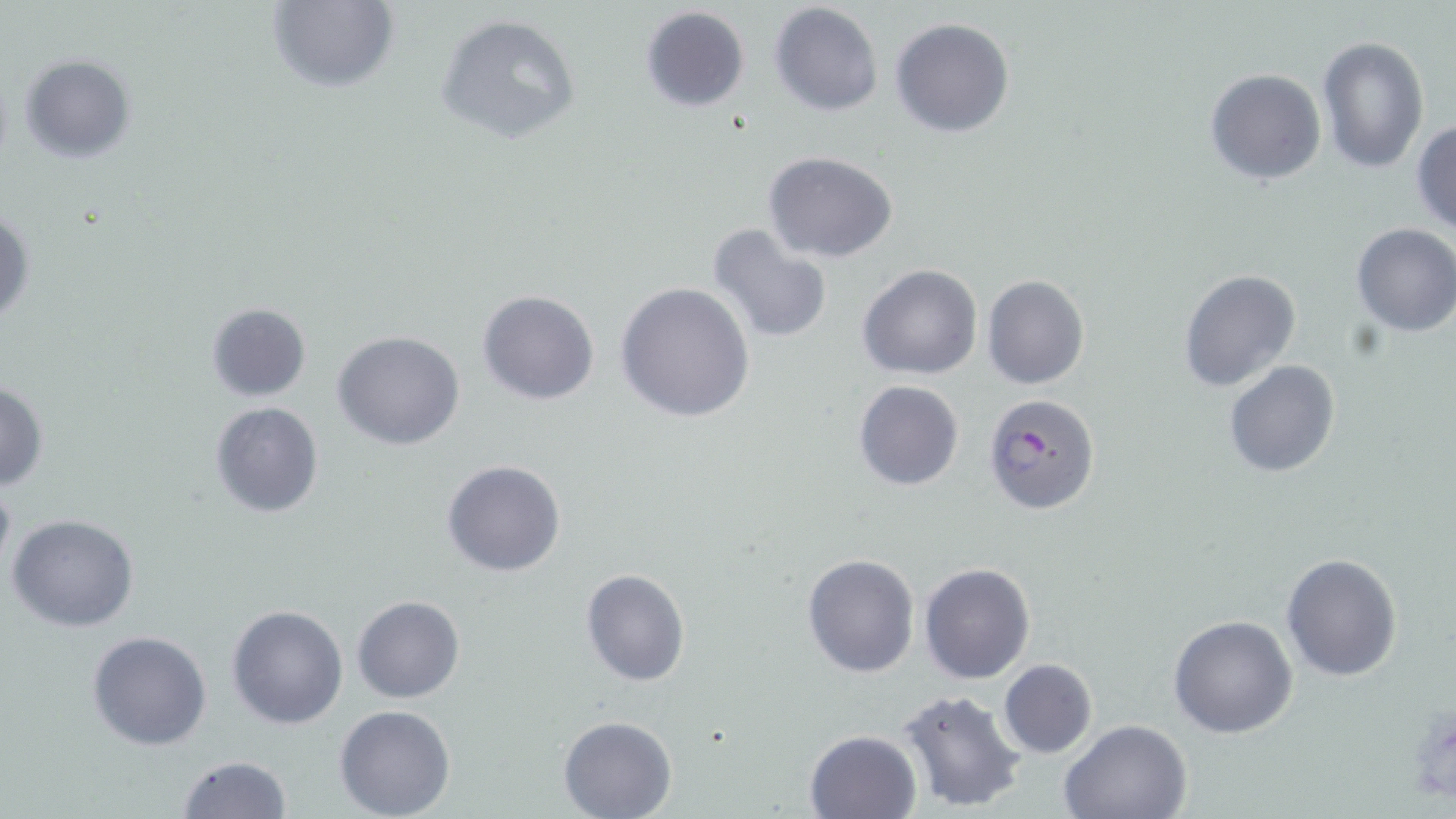

Summary:
  - Coordinate format: approximate bounding boxes as (x1, y1, x2, y2) in pixels
  - Plasmodium falciparum-infected red blood cell locations: (984, 393, 1100, 514)
  - Uninfected red blood cell locations: (265, 0, 400, 94), (770, 2, 883, 116), (640, 6, 750, 113), (434, 13, 582, 144), (890, 17, 1015, 137), (1316, 36, 1430, 174), (18, 53, 136, 164), (1204, 68, 1326, 185), (1411, 118, 1456, 236), (762, 151, 899, 261), (1, 204, 34, 332), (1350, 222, 1456, 337), (706, 223, 834, 343), (858, 265, 983, 380), (1178, 268, 1301, 393), (981, 275, 1089, 390), (615, 282, 755, 422), (476, 289, 600, 405), (206, 302, 310, 401), (331, 330, 466, 451), (1223, 359, 1341, 478), (853, 380, 964, 491), (1, 381, 48, 489), (209, 401, 324, 518), (441, 459, 566, 577), (6, 513, 140, 633), (1280, 552, 1402, 683), (801, 553, 920, 677), (920, 561, 1035, 684), (580, 569, 689, 685), (353, 595, 465, 703), (225, 604, 349, 730), (1167, 614, 1298, 739), (86, 630, 213, 751), (997, 659, 1097, 758), (897, 687, 1029, 813), (335, 703, 456, 819), (557, 716, 677, 819), (1058, 718, 1191, 819), (805, 729, 920, 818), (175, 755, 290, 819)
  - Slide-level diagnosis: Plasmodium falciparum
  - Field of view: single
  - Preparation: thin blood film
  - Image size: 1456×819 pixels
  - Magnification: 1000x
  - Stain: May-Grünwald-Giemsa
  - Modality: optical microscopy